Report the malaria status of this cell.
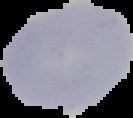

It is uninfected.

Cell region segmented out of the field of view; the surrounding area is masked to black. From a thin blood film. Image is 133×118 pixels.